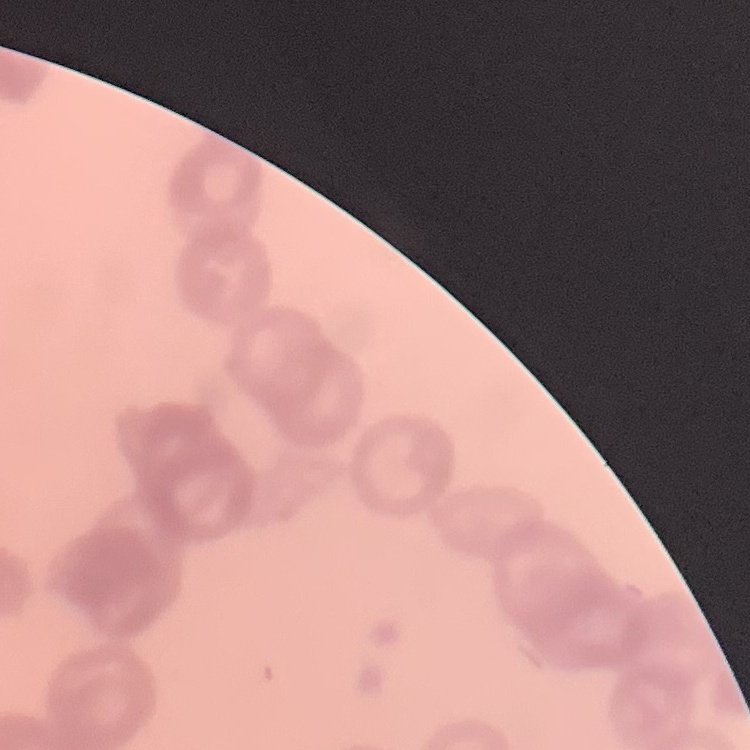
Summary:
  - Red blood cell morphology: rouleaux formation
  - Preparation: thin peripheral smear
  - Stain: Field's or Giemsa
  - Image type: one tile cut from a larger photomicrograph